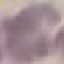
malaria_status: uninfected
preparation: thin blood smear
stain: Giemsa
image_type: automatically extracted cell patch, resized to 64 × 64 pixels
capture: smartphone camera at the microscope eyepiece